State which parasite is depicted.
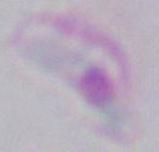

This is Toxoplasma gondii.

magnification = 1000x
modality = micrograph